Comment on the morphology of the erythrocytes.
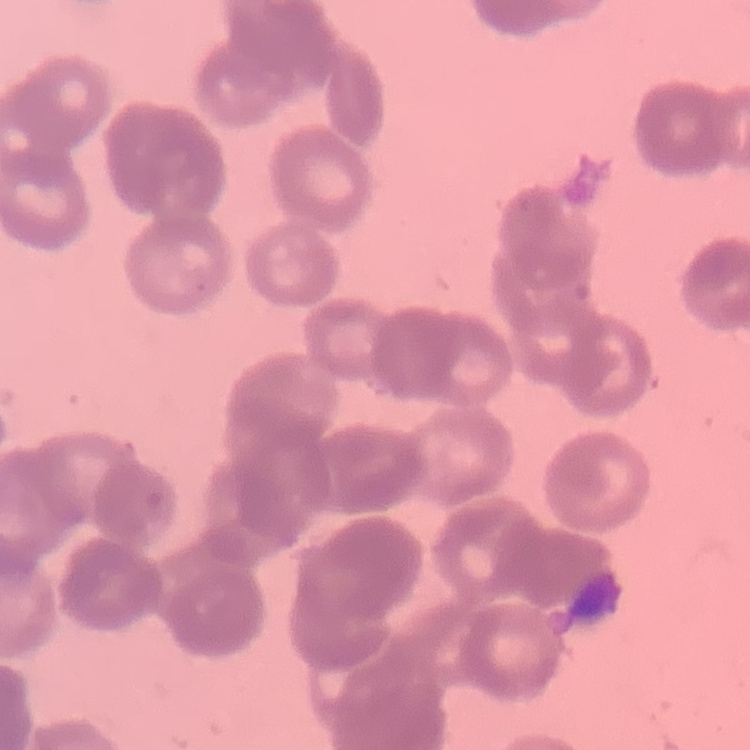

They show rouleaux formation.

Square crop of a larger photomicrograph. Stained with either Field's or Giemsa. Thin blood smear.